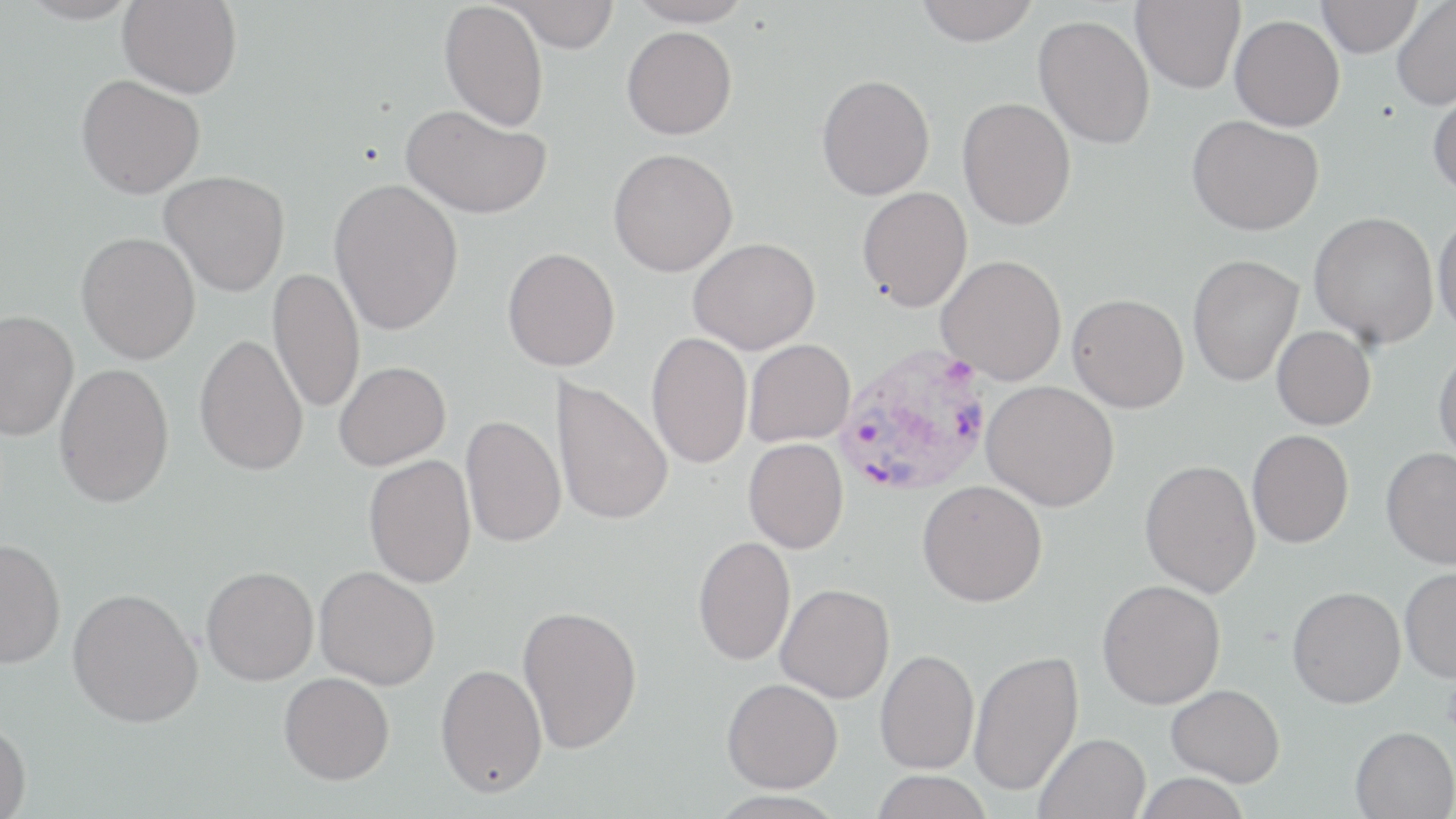

slide_level_diagnosis: Plasmodium vivax
platelet_locations: 'approximate bounding boxes as named x1/y1/x2/y2 corners in pixels: (x1=1442, y1=678, x2=1456, y2=734)'
field_of_view: single
stain: May-Grünwald-Giemsa
image_size: 1456×819 pixels
preparation: thin blood smear
plasmodium_vivax_infected_red_blood_cell_locations: 'approximate bounding boxes as named x1/y1/x2/y2 corners in pixels: (x1=833, y1=343, x2=995, y2=500)'
magnification: 1000x
modality: optical microscopy
uninfected_red_blood_cell_locations: 'approximate bounding boxes as named x1/y1/x2/y2 corners in pixels: (x1=14, y1=0, x2=142, y2=25), (x1=118, y1=0, x2=242, y2=98), (x1=497, y1=0, x2=621, y2=52), (x1=628, y1=0, x2=753, y2=27), (x1=1131, y1=0, x2=1245, y2=93), (x1=1316, y1=0, x2=1423, y2=57), (x1=439, y1=1, x2=548, y2=131), (x1=914, y1=1, x2=1040, y2=45), (x1=1392, y1=1, x2=1456, y2=110), (x1=1034, y1=14, x2=1155, y2=150), (x1=1230, y1=15, x2=1344, y2=131), (x1=621, y1=25, x2=737, y2=139), (x1=816, y1=74, x2=935, y2=200), (x1=76, y1=75, x2=204, y2=198), (x1=1428, y1=86, x2=1456, y2=199), (x1=956, y1=97, x2=1076, y2=230), (x1=400, y1=104, x2=551, y2=219), (x1=1187, y1=115, x2=1324, y2=235), (x1=608, y1=148, x2=738, y2=276), (x1=159, y1=170, x2=289, y2=297), (x1=328, y1=178, x2=464, y2=336), (x1=857, y1=186, x2=972, y2=311), (x1=1309, y1=211, x2=1439, y2=348), (x1=1433, y1=211, x2=1456, y2=341), (x1=76, y1=232, x2=200, y2=364), (x1=688, y1=237, x2=820, y2=354), (x1=502, y1=247, x2=620, y2=370), (x1=936, y1=254, x2=1067, y2=385), (x1=1187, y1=254, x2=1304, y2=386), (x1=267, y1=267, x2=365, y2=414), (x1=1067, y1=293, x2=1189, y2=412), (x1=0, y1=310, x2=79, y2=442), (x1=1272, y1=326, x2=1376, y2=430), (x1=646, y1=332, x2=752, y2=469), (x1=194, y1=334, x2=308, y2=476), (x1=744, y1=338, x2=855, y2=446), (x1=1433, y1=346, x2=1456, y2=465), (x1=333, y1=361, x2=451, y2=470), (x1=54, y1=362, x2=174, y2=508), (x1=551, y1=378, x2=674, y2=526), (x1=982, y1=380, x2=1119, y2=511), (x1=460, y1=415, x2=566, y2=547), (x1=1247, y1=429, x2=1354, y2=548), (x1=743, y1=438, x2=849, y2=553), (x1=1381, y1=447, x2=1456, y2=569), (x1=364, y1=454, x2=476, y2=588), (x1=1140, y1=458, x2=1261, y2=597), (x1=918, y1=480, x2=1048, y2=606), (x1=693, y1=535, x2=796, y2=666), (x1=0, y1=537, x2=66, y2=668), (x1=202, y1=566, x2=319, y2=685), (x1=314, y1=566, x2=440, y2=690), (x1=1400, y1=566, x2=1456, y2=682), (x1=1097, y1=579, x2=1225, y2=709), (x1=775, y1=583, x2=895, y2=703), (x1=1287, y1=585, x2=1406, y2=708), (x1=67, y1=587, x2=203, y2=727), (x1=517, y1=604, x2=643, y2=754), (x1=874, y1=649, x2=979, y2=775), (x1=968, y1=650, x2=1083, y2=796), (x1=435, y1=663, x2=547, y2=798), (x1=279, y1=672, x2=394, y2=785), (x1=722, y1=678, x2=843, y2=793), (x1=1166, y1=684, x2=1285, y2=786), (x1=0, y1=721, x2=31, y2=818), (x1=1350, y1=725, x2=1456, y2=818), (x1=1034, y1=732, x2=1151, y2=819), (x1=871, y1=770, x2=992, y2=818), (x1=1132, y1=772, x2=1252, y2=819), (x1=708, y1=791, x2=847, y2=818)'